Give the extent of all Plasmodium falciparum-infected red blood cells.
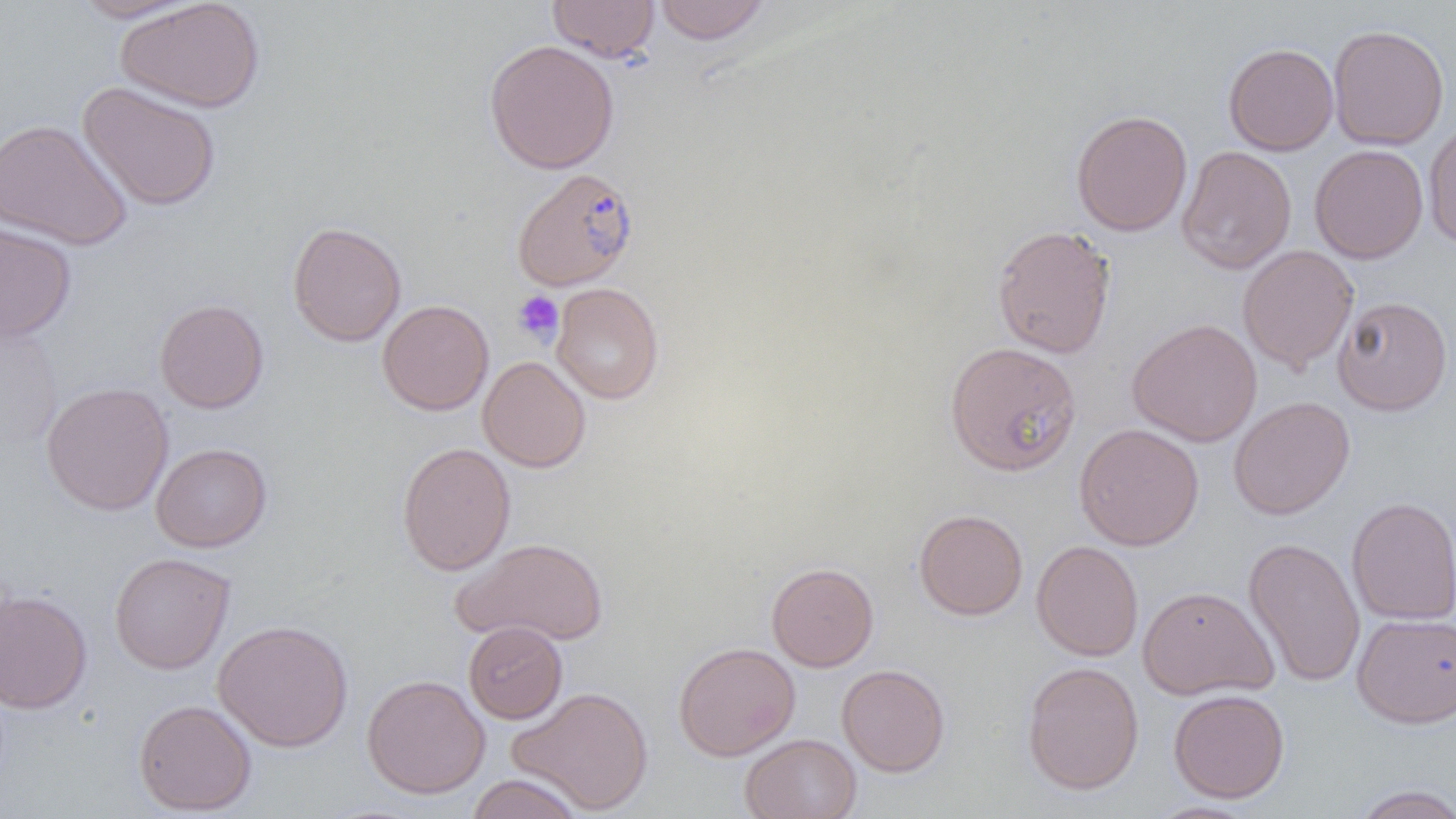
Approximate bounding boxes as [x1, y1, x2, y2] in pixels.
Plasmodium falciparum-infected red blood cells: [512, 168, 639, 291].

Platelet locations: [512, 291, 564, 345]. Uninfected red blood cell locations: [69, 0, 200, 23], [115, 0, 265, 113], [548, 1, 660, 63], [654, 1, 770, 45], [1328, 24, 1449, 150], [483, 39, 620, 174], [1223, 42, 1338, 155], [78, 81, 222, 212], [1071, 109, 1192, 236], [0, 118, 132, 251], [1423, 120, 1456, 248], [1309, 144, 1428, 264], [1177, 145, 1297, 274], [0, 221, 77, 342], [287, 221, 407, 347], [992, 224, 1116, 359], [1237, 244, 1359, 374], [551, 282, 664, 404], [1332, 295, 1453, 415], [154, 298, 269, 413], [377, 299, 494, 416], [1126, 318, 1263, 447], [0, 319, 64, 452], [944, 341, 1082, 476], [478, 356, 591, 472], [41, 382, 174, 516], [1228, 396, 1355, 520], [1074, 423, 1204, 550], [151, 442, 272, 552], [396, 442, 516, 575], [1346, 496, 1456, 625], [913, 509, 1028, 620], [1243, 536, 1365, 688], [452, 537, 609, 645], [1031, 540, 1144, 661], [109, 551, 235, 674], [766, 562, 879, 671], [1137, 585, 1278, 700], [0, 588, 92, 714], [1352, 613, 1456, 728], [213, 619, 353, 752], [463, 621, 568, 723], [673, 642, 800, 761], [1022, 661, 1144, 795], [836, 663, 950, 777], [361, 674, 490, 799], [508, 686, 654, 815], [1168, 688, 1289, 803], [133, 698, 257, 815], [740, 733, 862, 818], [463, 774, 586, 818], [1349, 784, 1456, 819]. Slide-level diagnosis: Plasmodium falciparum. Optical microscopy. Thin blood smear. Captured at 1000x magnification. Single field of view. Image is 1456×819 pixels.